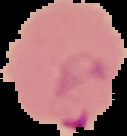
Segmented cell region on a black background. From a thin blood smear. Result: malaria parasites identified. Image is 127×136 pixels.